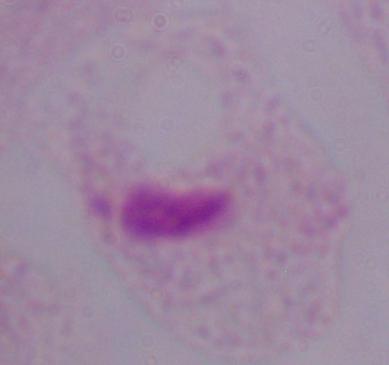

modality = photomicrograph
magnification = 1000x
identification = trichomonad